Assess this cell for malaria.
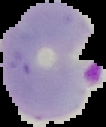

It is parasitized.

From a thin blood film. The area outside the segmented cell region is set to black. Image is 106×127 pixels.